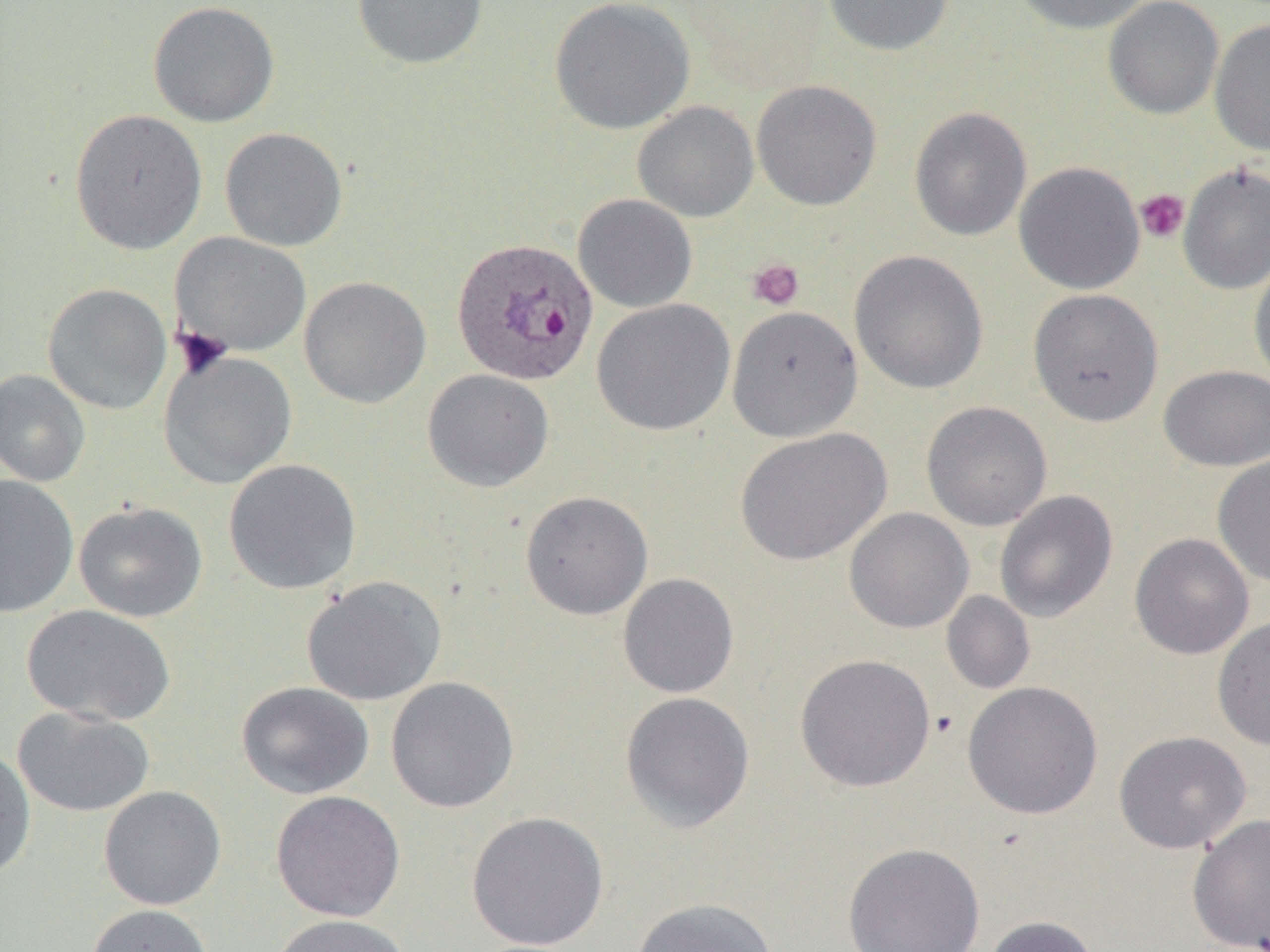

slide-level diagnosis = Plasmodium ovale
magnification = 1000x
image size = 1270×952 pixels
preparation = thin blood film
field of view = single
modality = light microscopy
uninfected red blood cell locations = approximate bounding boxes as [x1, y1, x2, y2] in pixels: [351, 0, 488, 70], [548, 0, 696, 135], [822, 0, 955, 56], [1010, 0, 1153, 34], [1103, 0, 1224, 119], [147, 1, 280, 127], [1209, 18, 1270, 155], [751, 79, 882, 211], [632, 101, 759, 223], [909, 107, 1032, 241], [69, 108, 207, 254], [220, 127, 348, 251], [1014, 161, 1145, 294], [1178, 163, 1270, 294], [573, 194, 698, 313], [172, 232, 312, 357], [849, 250, 989, 394], [1249, 256, 1270, 391], [299, 276, 432, 408], [42, 283, 172, 415], [1028, 288, 1164, 426], [591, 298, 736, 437], [726, 305, 863, 442], [158, 350, 297, 489], [1158, 365, 1270, 471], [0, 369, 91, 487], [421, 369, 554, 492], [921, 401, 1052, 531], [735, 427, 891, 566], [1212, 455, 1270, 587], [223, 458, 362, 595], [0, 475, 79, 617], [994, 490, 1118, 623], [520, 491, 653, 620], [73, 501, 207, 622], [844, 508, 974, 633], [1129, 533, 1255, 660], [617, 573, 739, 698], [302, 575, 447, 705], [941, 590, 1035, 695], [21, 604, 176, 726], [1211, 615, 1270, 751], [795, 653, 936, 792], [385, 677, 519, 813], [236, 681, 374, 799], [962, 681, 1103, 819], [620, 691, 755, 832], [12, 706, 155, 817], [1113, 730, 1251, 854], [0, 746, 36, 880], [98, 785, 226, 910], [271, 790, 405, 922], [466, 810, 609, 951], [1187, 813, 1270, 952], [842, 842, 985, 952], [631, 898, 778, 952], [85, 903, 214, 952], [268, 913, 414, 952], [983, 915, 1099, 952]
platelet locations = approximate bounding boxes as [x1, y1, x2, y2] in pixels: [1135, 189, 1189, 243], [747, 258, 805, 310]
Plasmodium ovale-infected red blood cell locations = approximate bounding boxes as [x1, y1, x2, y2] in pixels: [450, 237, 599, 387]